Point out each Plasmodium parasite.
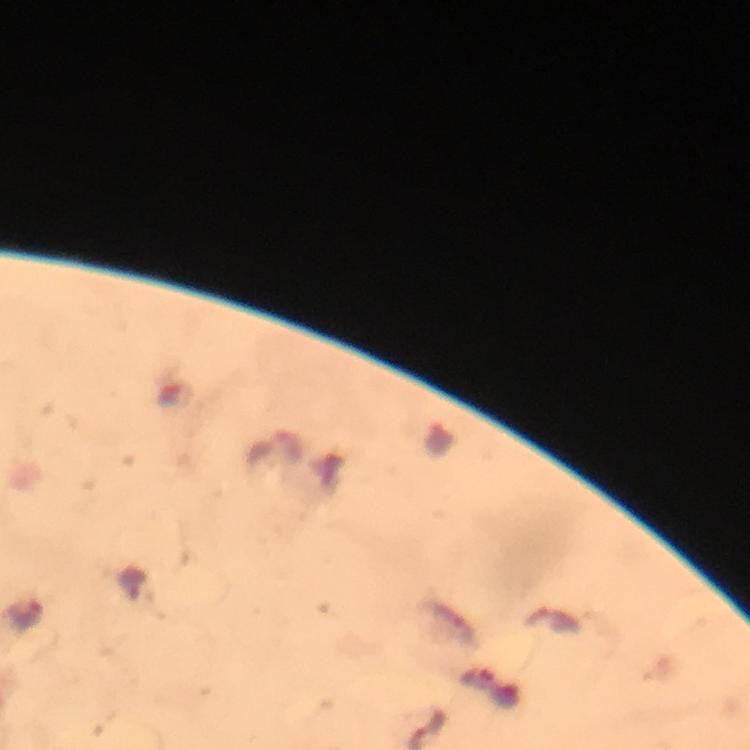

Approximate centers as (x, y) in pixels.
Plasmodium parasites: (552, 621).

{
  "immersion_oil": "used",
  "image_size": "750×750 pixels",
  "context": "from a malaria diagnostic workup",
  "cropped_from": "a single field of view",
  "magnification": "100x",
  "capture": "smartphone camera through the microscope",
  "preparation": "thick blood smear",
  "stain": "Giemsa"
}